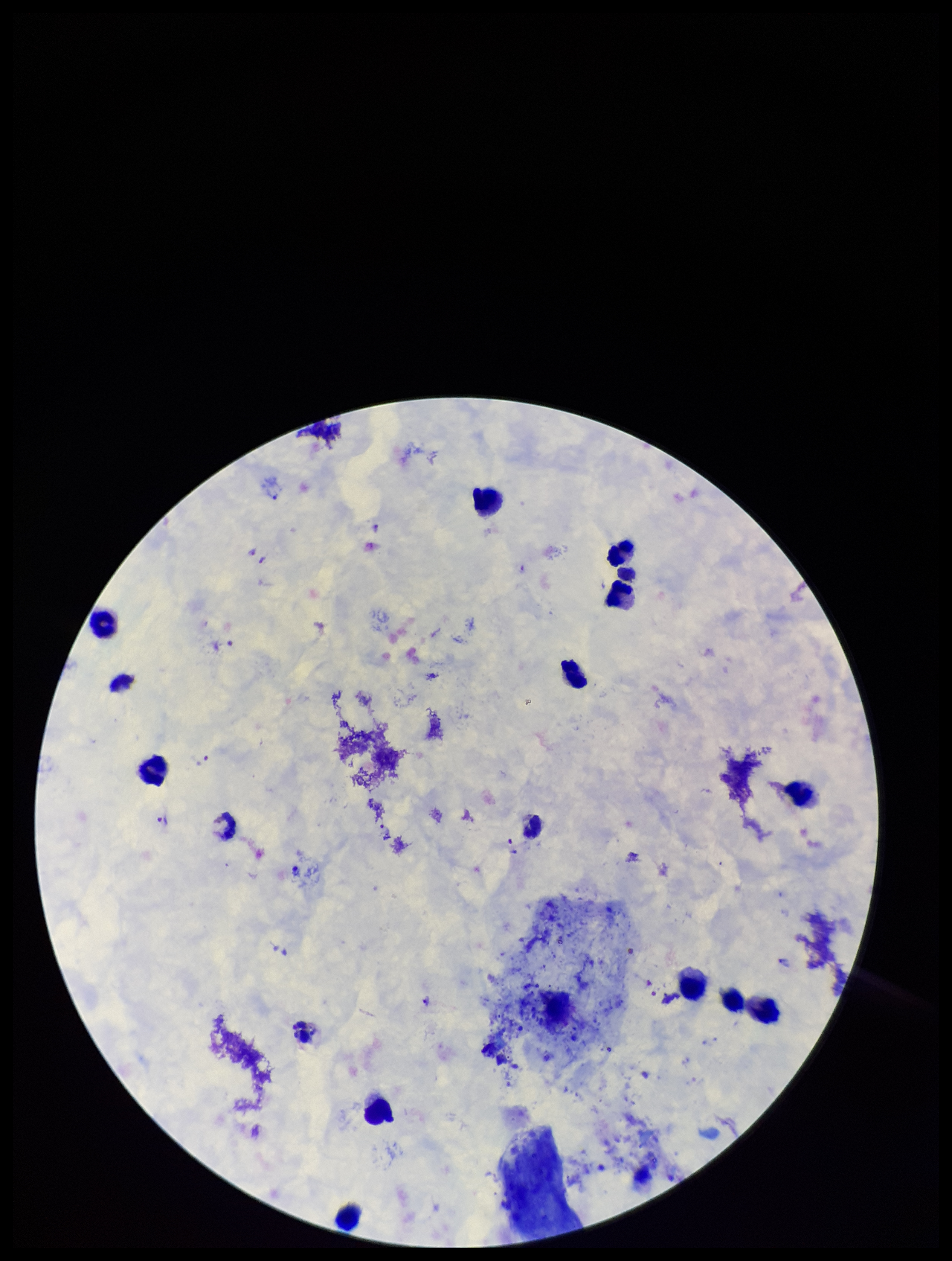

preparation = thick
Plasmodium parasites = identified
species reported for this patient = Plasmodium vivax
image size = 952×1261 pixels
leukocyte count = 15
patient malaria status = positive
parasite count = 19
capture = smartphone photograph through the microscope eyepiece
stain = Giemsa
field of view = one from this slide